Comment on the morphology of the red blood cells.
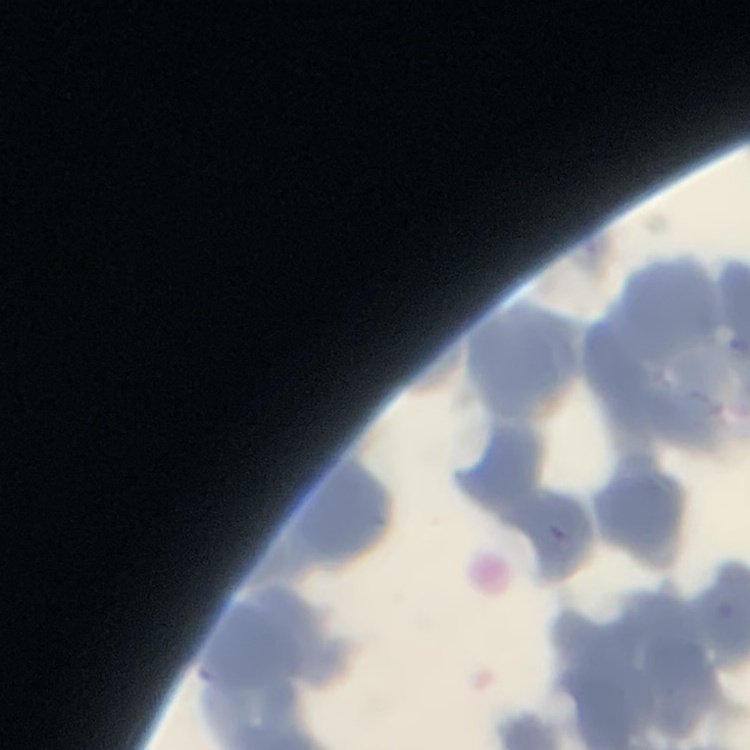

Rouleaux formation.

Field's or Giemsa stain. One tile cut from a larger photomicrograph. Thin peripheral smear.